Report the malaria status of this cell.
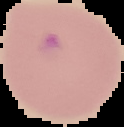

It is parasitized.

image_size: 124×127 pixels
image_type: segmented cell region with the area outside set to black
preparation: thin blood smear